Assess this cell for malaria.
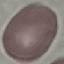

Uninfected.

{
  "image_type": "cell patch, automatically extracted from a larger field of view and resized to 64 × 64 pixels",
  "preparation": "thin smear",
  "capture": "smartphone camera at the microscope eyepiece",
  "stain": "Giemsa"
}